Identify the parasite.
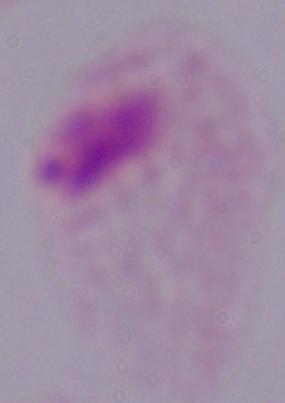

This is a trichomonad.

modality: micrograph
magnification: 1000x